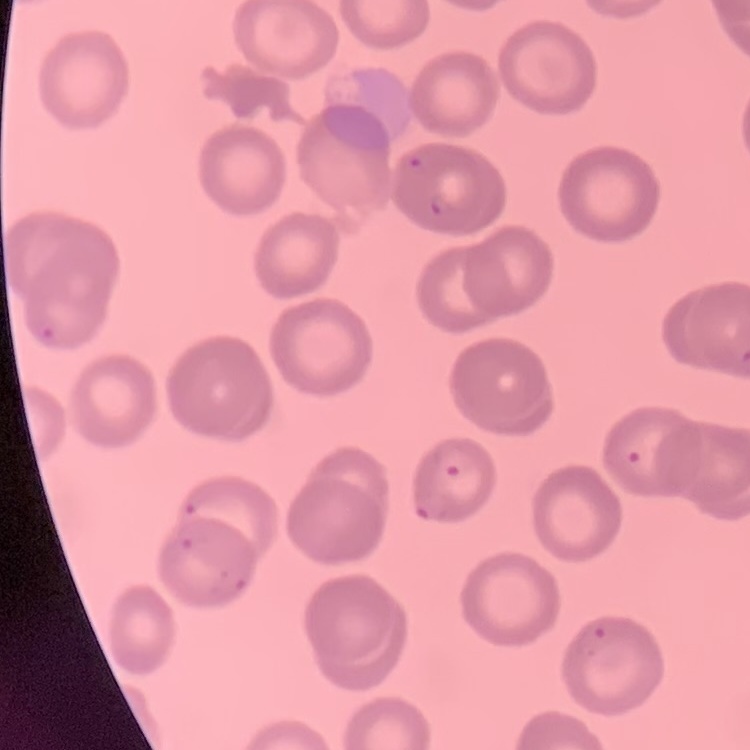 The red blood cells exhibit no rouleaux formation. Thin peripheral smear. Square crop of a larger photomicrograph. Stained with either Field's or Giemsa.